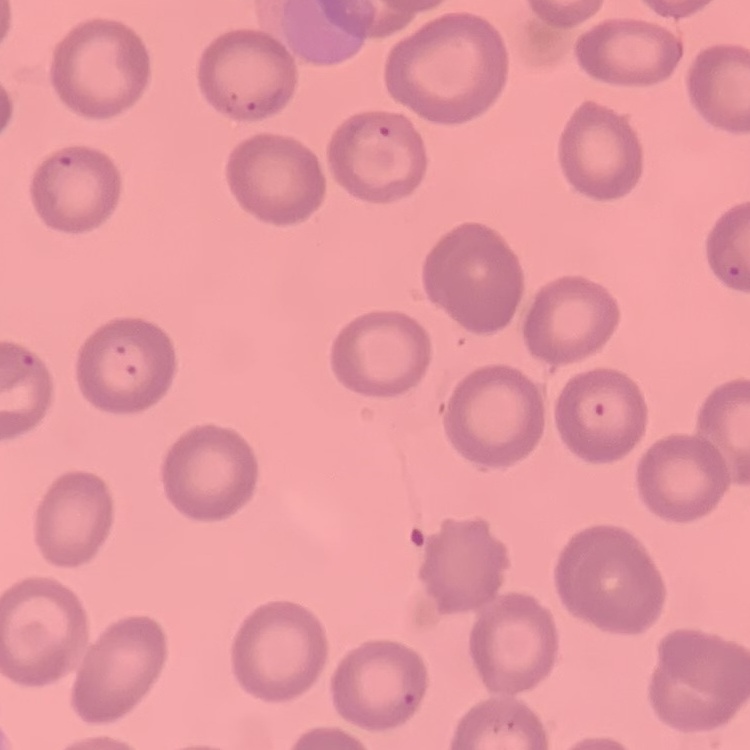
Summary:
  - Red blood cell morphology: no rouleaux formation
  - Stain: Field's or Giemsa
  - Image type: one tile cut from a larger photomicrograph
  - Preparation: thin peripheral smear